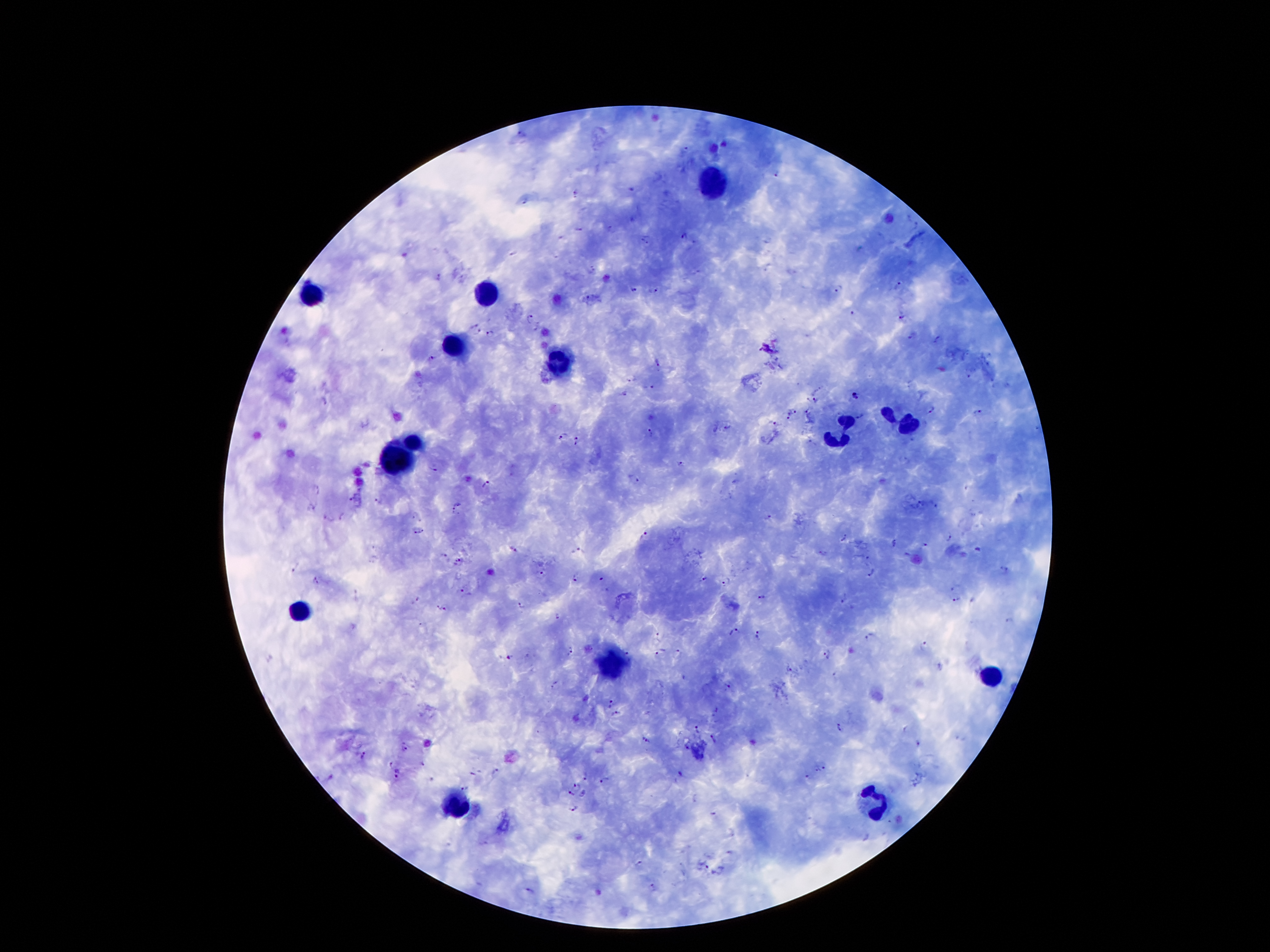

Approximate object centers, in pixels from the top-left corner. Malaria parasite locations: (x=685, y=149), (x=776, y=173), (x=632, y=189), (x=576, y=193), (x=524, y=202), (x=917, y=227), (x=578, y=228), (x=609, y=228), (x=685, y=235), (x=648, y=240), (x=438, y=277), (x=899, y=284), (x=839, y=289), (x=634, y=290), (x=653, y=290), (x=588, y=297), (x=852, y=313), (x=902, y=314), (x=531, y=319), (x=473, y=325), (x=479, y=331), (x=491, y=333), (x=913, y=336), (x=938, y=340), (x=431, y=358), (x=656, y=363), (x=969, y=375), (x=631, y=379), (x=649, y=387), (x=623, y=395), (x=854, y=396), (x=815, y=399), (x=325, y=400), (x=931, y=410), (x=977, y=411), (x=795, y=412), (x=809, y=412), (x=861, y=414), (x=787, y=417), (x=771, y=422), (x=729, y=425), (x=649, y=432), (x=562, y=435), (x=575, y=437), (x=577, y=443), (x=680, y=463), (x=434, y=468), (x=635, y=478), (x=487, y=484), (x=317, y=488), (x=351, y=499), (x=378, y=500), (x=921, y=502), (x=457, y=504), (x=936, y=505), (x=453, y=511), (x=415, y=514), (x=326, y=517), (x=342, y=517), (x=769, y=517), (x=418, y=532), (x=645, y=534), (x=949, y=537), (x=846, y=538), (x=894, y=542), (x=925, y=543), (x=515, y=548), (x=578, y=551), (x=444, y=556), (x=869, y=558), (x=461, y=559), (x=295, y=566), (x=1005, y=569), (x=542, y=574), (x=872, y=574), (x=575, y=577), (x=705, y=579), (x=319, y=580), (x=601, y=580), (x=726, y=580), (x=460, y=590), (x=415, y=597), (x=764, y=597), (x=974, y=598), (x=841, y=600), (x=956, y=600), (x=520, y=605), (x=437, y=607), (x=445, y=610), (x=558, y=616), (x=1011, y=621), (x=734, y=630), (x=659, y=635), (x=758, y=635), (x=868, y=638), (x=925, y=647), (x=572, y=649), (x=659, y=651), (x=680, y=652), (x=627, y=653), (x=829, y=654), (x=509, y=657), (x=791, y=668), (x=557, y=685), (x=727, y=686), (x=612, y=704), (x=715, y=710), (x=615, y=713), (x=841, y=726), (x=697, y=728), (x=646, y=738), (x=713, y=739), (x=404, y=745), (x=919, y=745), (x=688, y=748), (x=365, y=754), (x=391, y=762), (x=422, y=764), (x=823, y=767), (x=397, y=769), (x=497, y=770), (x=815, y=771), (x=473, y=772), (x=680, y=773), (x=397, y=777), (x=585, y=777), (x=808, y=777), (x=605, y=779), (x=577, y=785), (x=465, y=787), (x=572, y=793), (x=583, y=794), (x=573, y=809), (x=712, y=811), (x=640, y=864), (x=704, y=865), (x=652, y=888), (x=529, y=890). Leukocyte locations: (x=713, y=182), (x=308, y=292), (x=485, y=292), (x=452, y=348), (x=560, y=363), (x=900, y=418), (x=839, y=436), (x=416, y=440), (x=399, y=462), (x=297, y=613), (x=613, y=661), (x=993, y=675), (x=874, y=803), (x=456, y=807). Thick blood smear. 100x magnification. Single field of view. Smartphone photograph taken through the microscope eyepiece. Image is 1270×952 pixels. Giemsa stain. Patient malaria status: positive for Plasmodium falciparum.